Assess the morphology of the red blood cells.
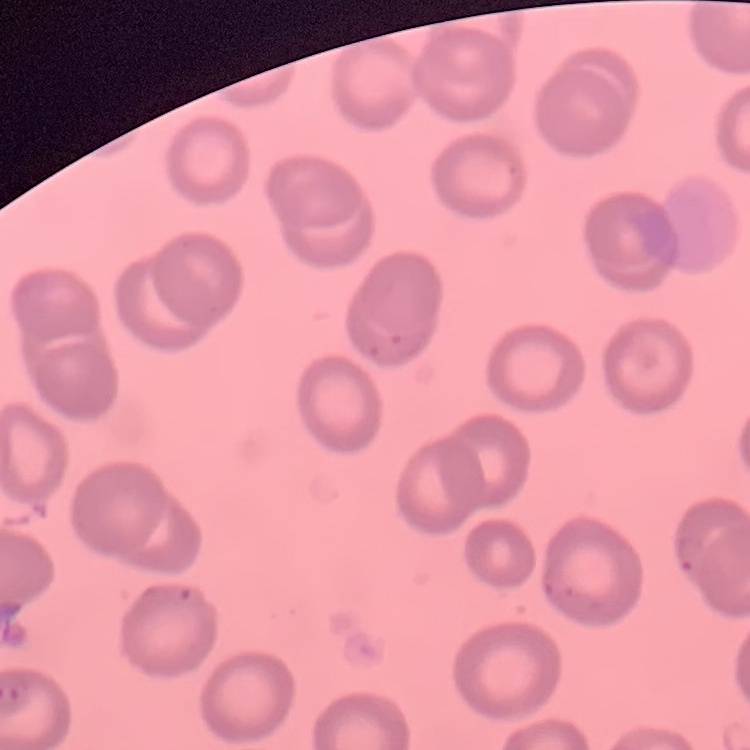

They show no rouleaux formation.

Thin peripheral smear. Field's or Giemsa stain. Square crop of a larger photomicrograph.